Give the position of every leukocyte visible.
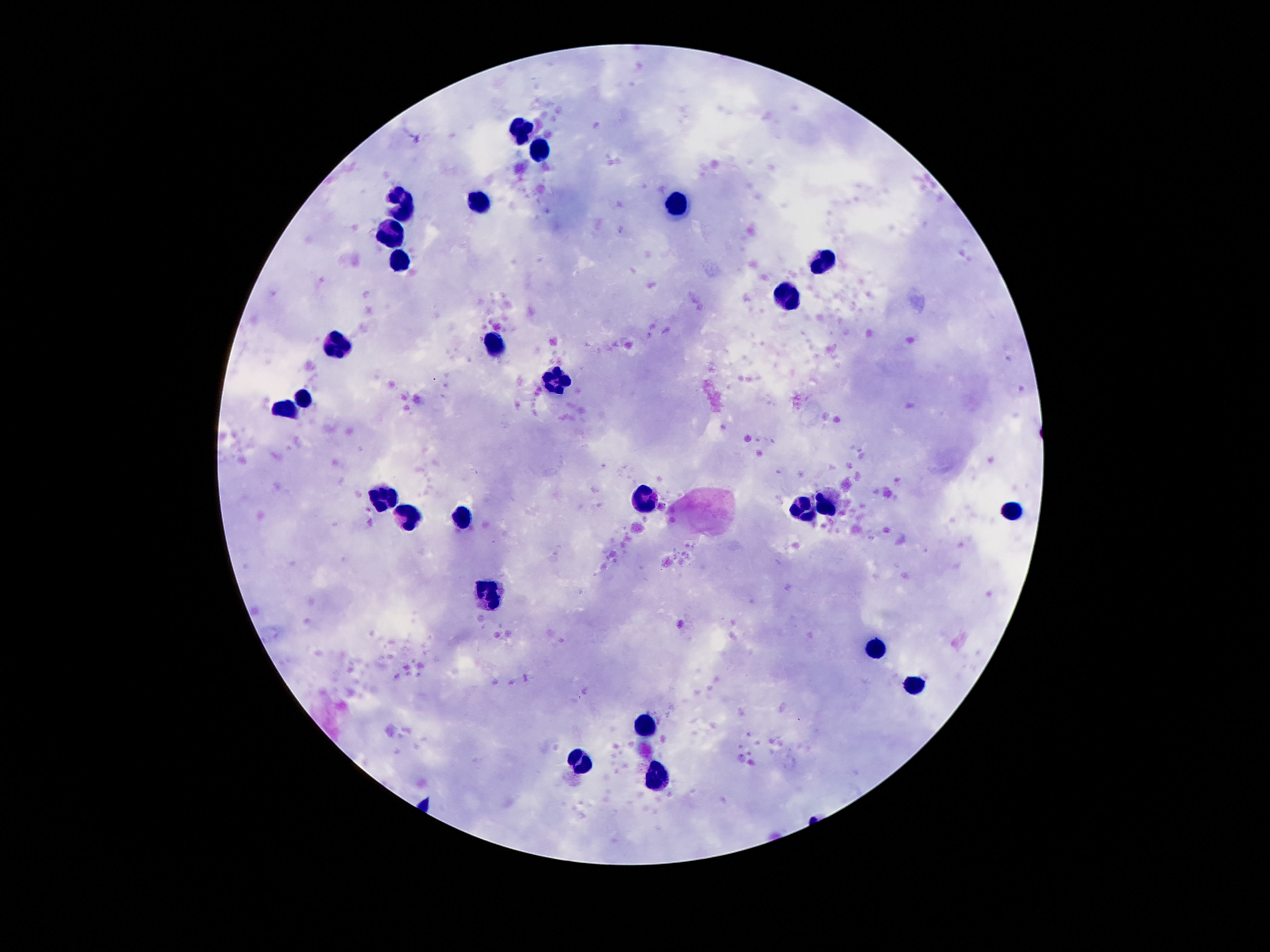

Approximate object centers, in pixels from the top-left corner.
Leukocytes: (x=522, y=129), (x=540, y=149), (x=480, y=203), (x=678, y=203), (x=402, y=204), (x=393, y=231), (x=402, y=260), (x=825, y=263), (x=788, y=298), (x=339, y=344), (x=496, y=345), (x=557, y=380), (x=303, y=399), (x=288, y=410), (x=643, y=499), (x=384, y=501), (x=827, y=505), (x=804, y=508), (x=1011, y=510), (x=407, y=515), (x=465, y=519), (x=491, y=592), (x=878, y=649), (x=913, y=683), (x=647, y=724), (x=580, y=763), (x=659, y=775).

Summary:
  - Preparation: thick blood smear
  - Capture: smartphone camera through the microscope eyepiece
  - Patient malaria status: negative
  - Stain: Giemsa
  - Magnification: 100x
  - Image size: 1270×952 pixels
  - Field of view: single